Identify the blood parasite species.
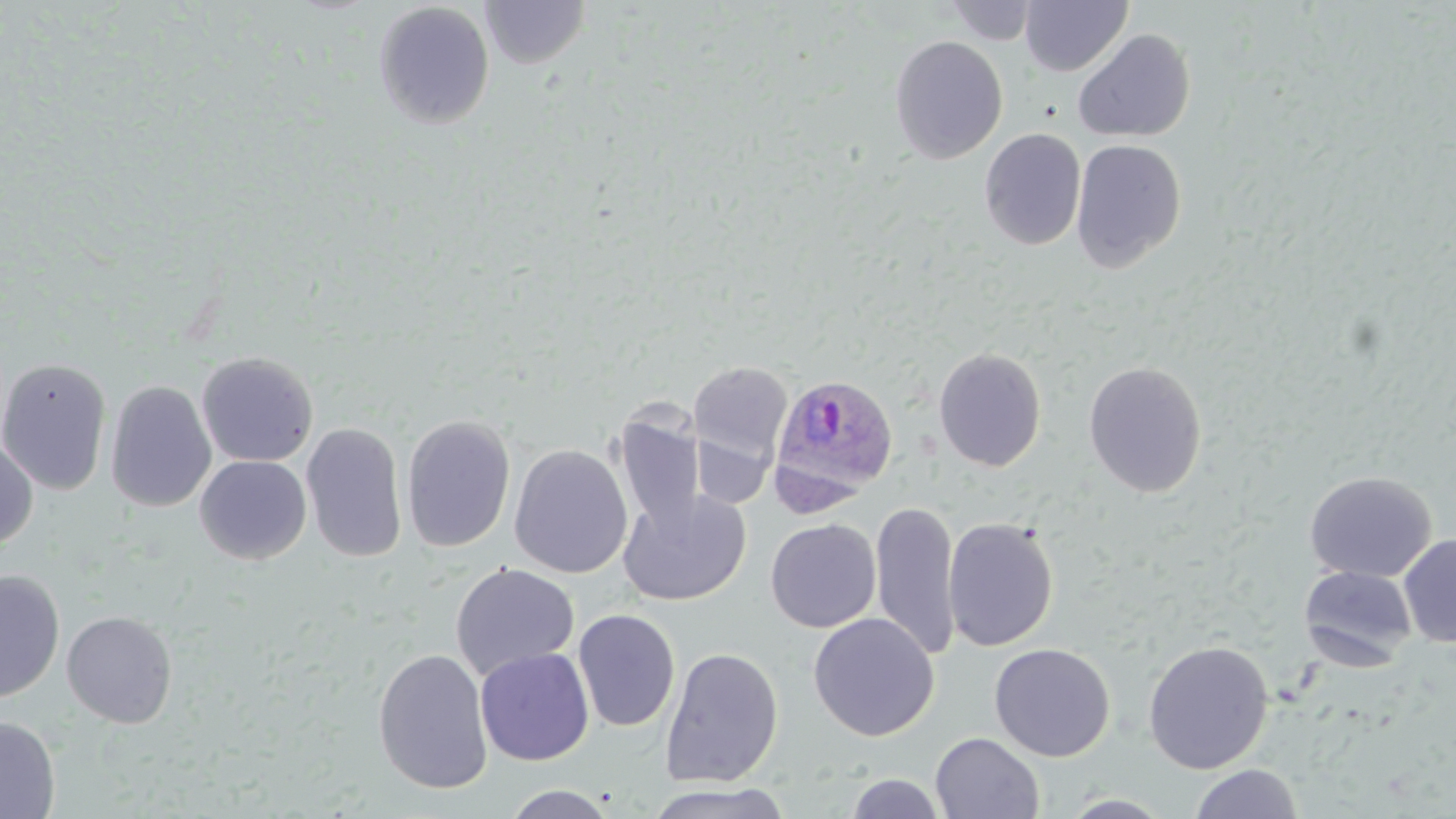

Plasmodium ovale.

Summary:
  - Coordinate format: approximate bounding boxes as (x1,y1)-(x2,y2) corner pairs in pixels
  - Plasmodium ovale-infected red blood cell locations: (769,373)-(898,504)
  - Uninfected red blood cell locations: (1019,0)-(1133,76), (373,1)-(495,130), (480,1)-(591,69), (944,1)-(1039,45), (1072,28)-(1196,143), (889,35)-(1008,164), (980,128)-(1086,250), (1071,139)-(1187,272), (933,348)-(1046,472), (196,351)-(318,467), (0,356)-(112,496), (689,361)-(793,468), (1083,361)-(1207,498), (105,379)-(217,513), (613,408)-(706,534), (401,414)-(516,554), (301,422)-(408,563), (691,427)-(775,511), (0,438)-(38,550), (508,444)-(632,579), (194,455)-(312,564), (1304,470)-(1436,582), (618,488)-(752,607), (871,501)-(962,660), (942,517)-(1059,652), (766,518)-(881,633), (1398,534)-(1456,647), (450,563)-(580,680), (1299,565)-(1418,670), (0,568)-(65,703), (572,608)-(681,732), (62,610)-(177,727), (808,612)-(939,741), (1142,639)-(1274,774), (989,642)-(1115,761), (659,646)-(784,787), (475,647)-(594,766), (372,648)-(494,795), (0,715)-(60,818), (930,732)-(1045,818), (1188,764)-(1305,819), (844,773)-(946,818), (642,783)-(796,819), (501,785)-(619,818), (1059,793)-(1178,818)
  - Magnification: 1000x
  - Stain: May-Grünwald-Giemsa
  - Preparation: thin blood smear
  - Image size: 1456×819 pixels
  - Modality: light microscopy
  - Field of view: one of a larger specimen